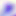

magnification: 400x
identification: Toxoplasma gondii
modality: photomicrograph